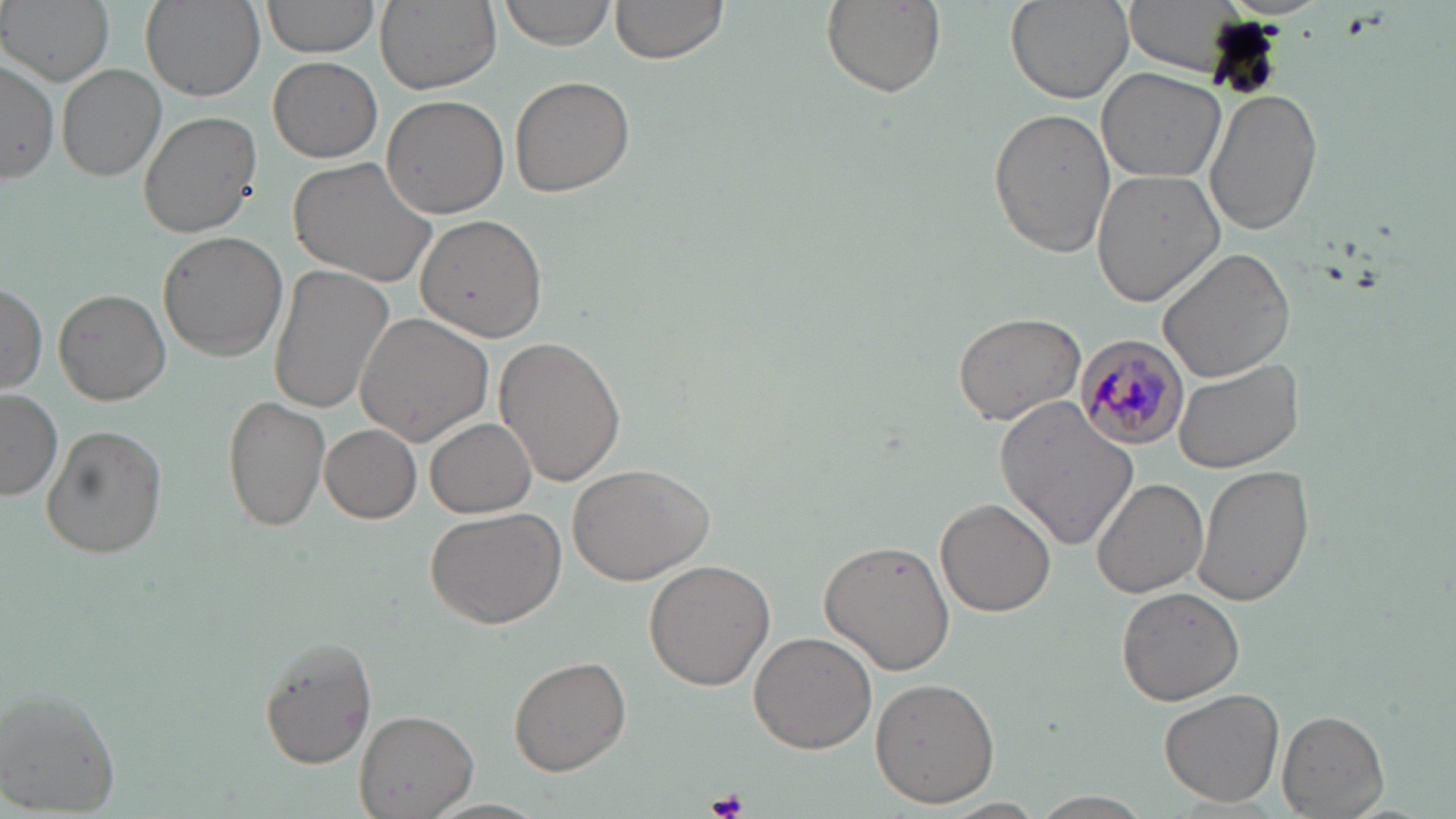
Approximate bounding boxes as (x1,y1)-(x2,y2) corner pairs in pixels. Platelet locations: (709,790)-(747,819). Plasmodium malariae-infected red blood cell locations: (1075,333)-(1189,450). Uninfected red blood cell locations: (2,0)-(115,86), (140,0)-(265,101), (260,0)-(381,61), (499,0)-(618,51), (606,0)-(729,67), (821,0)-(943,97), (1004,0)-(1132,105), (1122,0)-(1244,72), (376,2)-(502,94), (268,57)-(382,163), (59,65)-(168,181), (1097,66)-(1226,184), (509,75)-(634,199), (1205,89)-(1323,236), (381,94)-(511,220), (987,106)-(1115,259), (138,107)-(261,239), (286,157)-(438,288), (1090,171)-(1225,304), (414,214)-(549,342), (157,231)-(288,360), (1159,245)-(1297,382), (268,264)-(395,413), (0,283)-(48,394), (55,289)-(171,405), (954,311)-(1086,427), (356,312)-(496,445), (493,335)-(626,488), (1172,359)-(1304,474), (0,389)-(62,500), (223,394)-(330,532), (995,395)-(1139,548), (426,418)-(536,518), (40,424)-(168,559), (319,424)-(422,524), (1192,462)-(1315,609), (566,463)-(715,586), (1091,477)-(1208,598), (936,499)-(1056,618), (426,505)-(566,627), (819,539)-(955,675), (643,559)-(775,690), (1116,587)-(1244,705), (749,631)-(876,753), (255,635)-(377,770), (511,653)-(632,776), (870,677)-(1001,808), (1,685)-(122,816), (1160,688)-(1285,807), (354,710)-(478,819), (1278,710)-(1389,816), (1028,791)-(1154,818). Slide-level diagnosis: Plasmodium malariae. Captured at 1000x magnification. Optical microscopy. May-Grünwald-Giemsa-stained preparation. Single field of view. Thin blood film. Image is 1456×819 pixels.